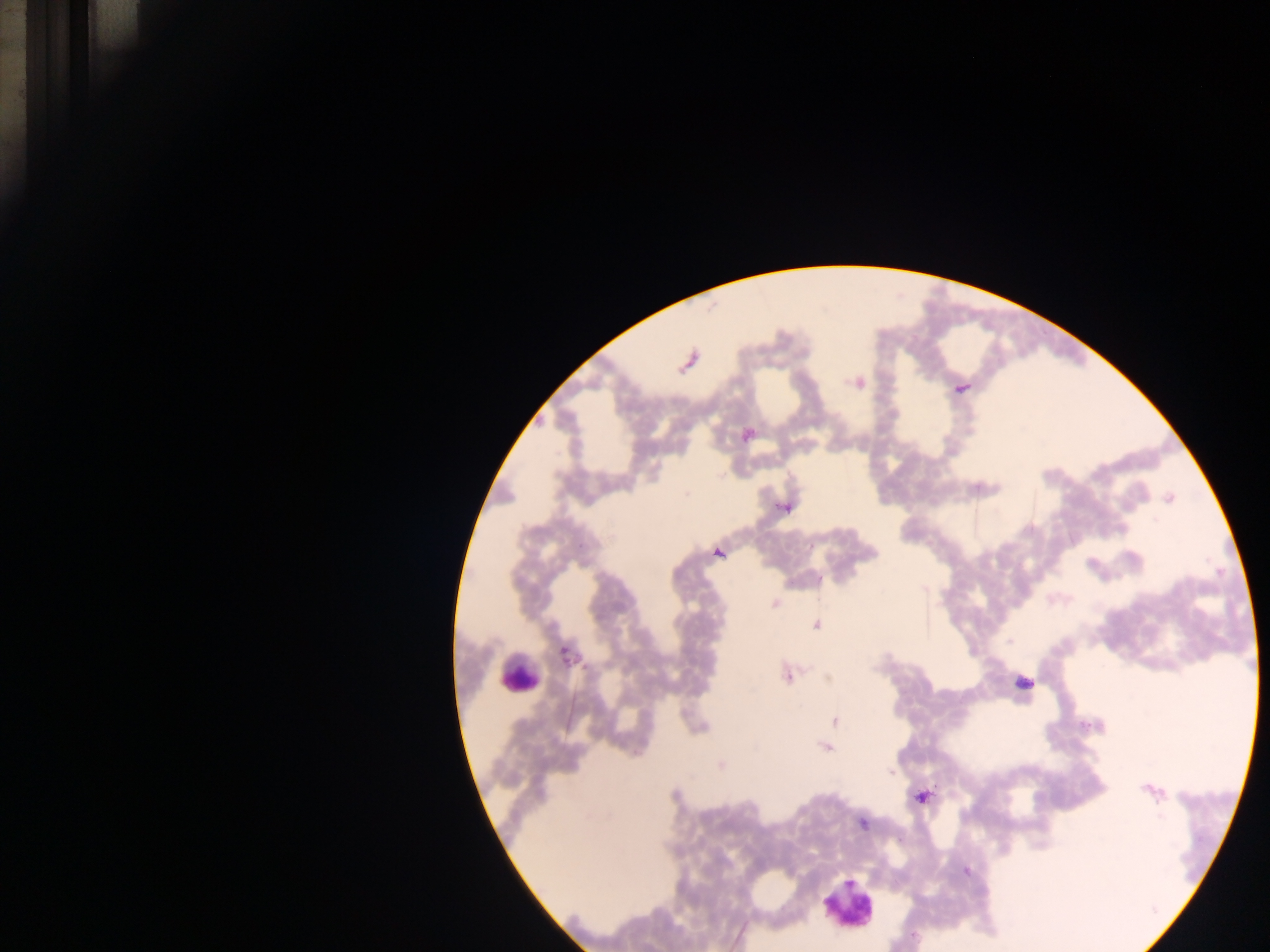

Approximate centers as [x, y] in pixels. Leukocyte locations: [518, 673], [1025, 684], [849, 905]. Plasmodium parasite locations: [961, 386], [786, 508], [720, 553], [923, 588], [774, 603], [815, 624], [1010, 642], [564, 654], [787, 676], [835, 720], [826, 748], [721, 764], [890, 772], [921, 796], [862, 824], [965, 871]. Image is 1270×952 pixels. Photographed through a microscope with a mobile-phone camera. Single field of view. Sample from Ghana. Thick blood film.